Outline each blood parasite and name the species.
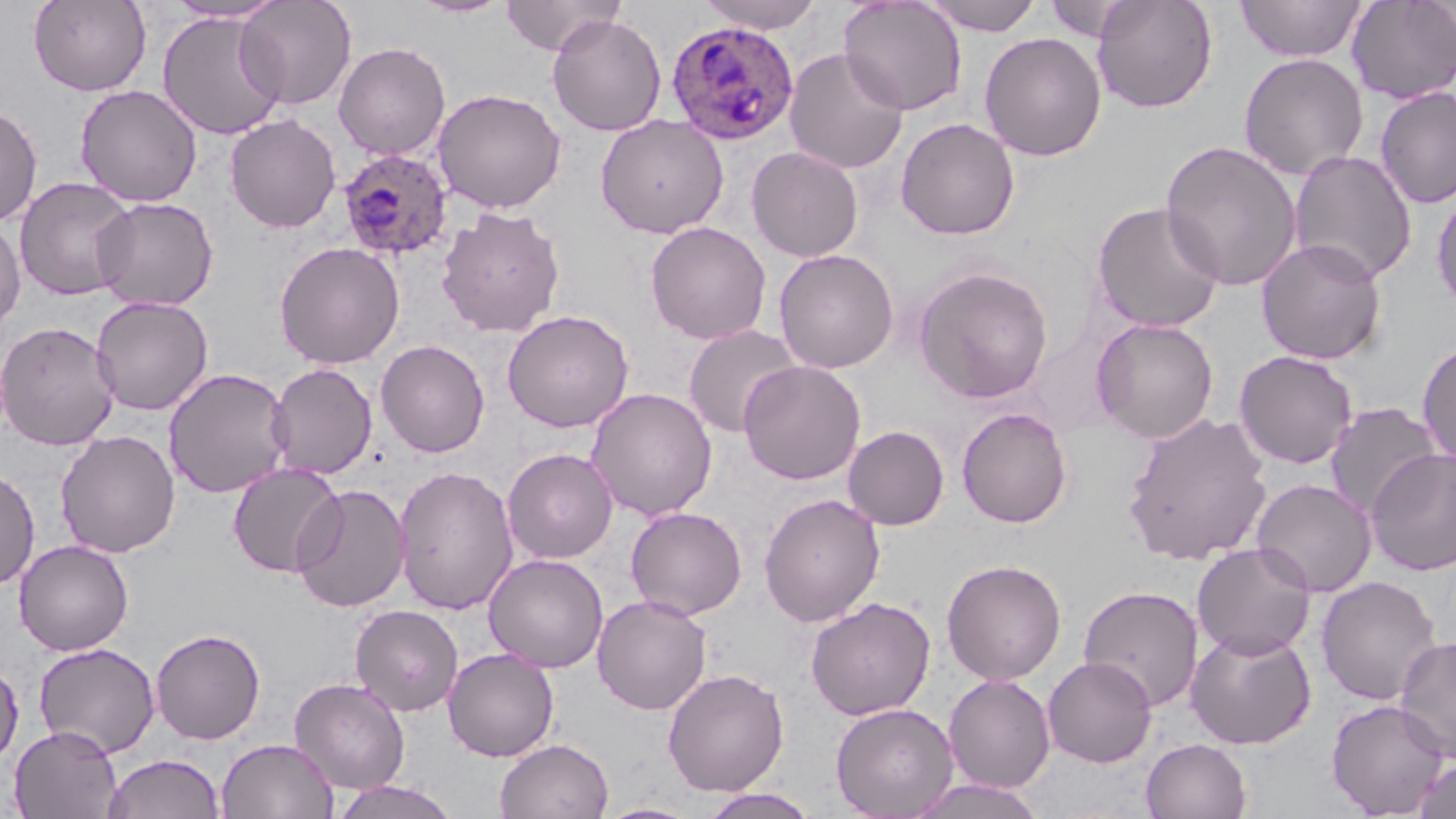

Approximate bounding boxes as (x1,y1)-(x2,y2) corner pairs in pixels.
Plasmodium ovale-infected red blood cells: (666,20)-(799,144), (337,147)-(453,260).
No Plasmodium falciparum, Plasmodium malariae, Plasmodium vivax, Babesia divergens, or Trypanosoma brucei observed.

Summary:
  - Uninfected red blood cell locations: (29,0)-(151,96), (236,0)-(357,110), (409,0)-(514,18), (500,0)-(626,56), (696,0)-(826,33), (920,0)-(1044,36), (1091,0)-(1218,113), (1346,0)-(1456,104), (165,1)-(288,23), (838,1)-(968,116), (1043,1)-(1147,42), (1235,1)-(1368,62), (157,11)-(287,141), (547,13)-(666,136), (979,32)-(1106,161), (333,42)-(450,160), (784,48)-(909,174), (1238,52)-(1369,181), (75,85)-(202,207), (1374,86)-(1456,209), (432,88)-(566,213), (0,102)-(42,226), (225,114)-(341,233), (595,115)-(729,238), (895,117)-(1020,239), (1160,140)-(1302,292), (747,146)-(864,262), (1288,150)-(1418,285), (14,177)-(138,301), (1430,185)-(1456,315), (91,197)-(219,311), (1092,201)-(1225,334), (437,207)-(565,337), (0,216)-(25,337), (645,222)-(771,344), (1256,237)-(1387,365), (274,241)-(405,369), (774,249)-(898,373), (914,266)-(1053,403), (90,296)-(214,415), (501,309)-(634,433), (1091,318)-(1219,443), (0,320)-(120,450), (683,324)-(803,438), (1417,338)-(1456,468), (376,340)-(490,457), (1234,350)-(1358,469), (738,360)-(866,485), (267,363)-(377,480), (164,367)-(293,499), (586,387)-(718,521), (1324,402)-(1444,520), (956,407)-(1073,528), (1122,412)-(1273,565), (843,425)-(949,530), (55,430)-(181,558), (502,448)-(618,563), (1366,448)-(1456,575), (227,462)-(346,578), (393,465)-(519,615), (0,466)-(40,590), (1251,478)-(1377,597), (291,484)-(411,613), (759,493)-(885,627), (625,506)-(748,619), (13,539)-(134,656), (1191,542)-(1316,660), (483,553)-(608,671), (941,559)-(1067,685), (1316,576)-(1442,706), (1078,585)-(1204,713), (592,594)-(712,714), (805,597)-(936,720), (350,604)-(464,716), (1185,627)-(1317,749), (150,628)-(266,744), (1394,635)-(1456,762), (33,642)-(160,758), (443,648)-(559,761), (1043,657)-(1157,767), (0,658)-(24,771), (662,669)-(789,796), (943,675)-(1056,793), (290,678)-(410,793), (1326,699)-(1451,817), (830,702)-(959,819), (9,725)-(123,819), (494,738)-(614,819), (217,739)-(338,819), (1141,739)-(1253,819), (103,753)-(225,819), (1412,757)-(1456,819), (909,778)-(1046,819), (331,779)-(461,819), (699,788)-(821,819), (596,802)-(703,819)
  - Slide-level diagnosis: Plasmodium ovale
  - Image size: 1456×819 pixels
  - Modality: optical microscopy
  - Stain: May-Grünwald-Giemsa
  - Preparation: thin blood film
  - Field of view: one of a larger specimen
  - Magnification: 1000x